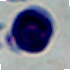
{
  "magnification": "1000x",
  "identification": "leukocyte",
  "modality": "micrograph"
}